Assess this cell for malaria.
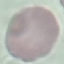

Uninfected.

Giemsa-stained preparation. Photographed with a smartphone camera at the microscope eyepiece. Thin blood film. Cell patch, automatically extracted from a larger field of view and resized to 64 × 64 pixels.